Classify this cell by malaria status.
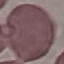

Uninfected.

Giemsa-stained preparation. Cell patch, automatically extracted from a larger field of view and resized to 64 × 64 pixels. Thin blood smear. Photographed with a smartphone camera at the microscope eyepiece.